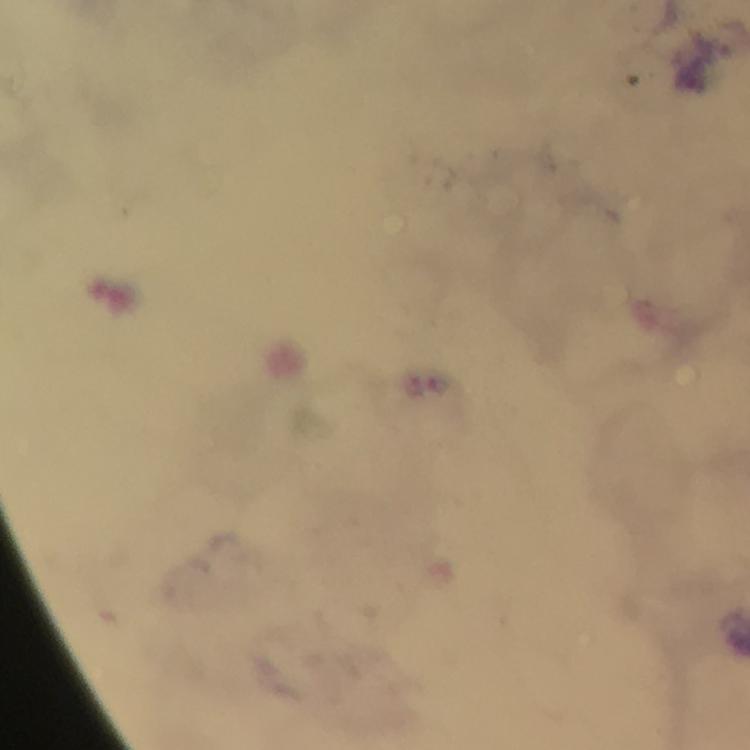

stain = Giemsa
image size = 750×750 pixels
magnification = 100x
Plasmodium parasite locations = approximate centers as {x, y} in pixels: {414, 386}
context = from a diagnostic examination for malaria
capture = smartphone camera through the microscope
cropped from = a single field of view
immersion oil = applied
preparation = thick smear